Point out each malaria parasite.
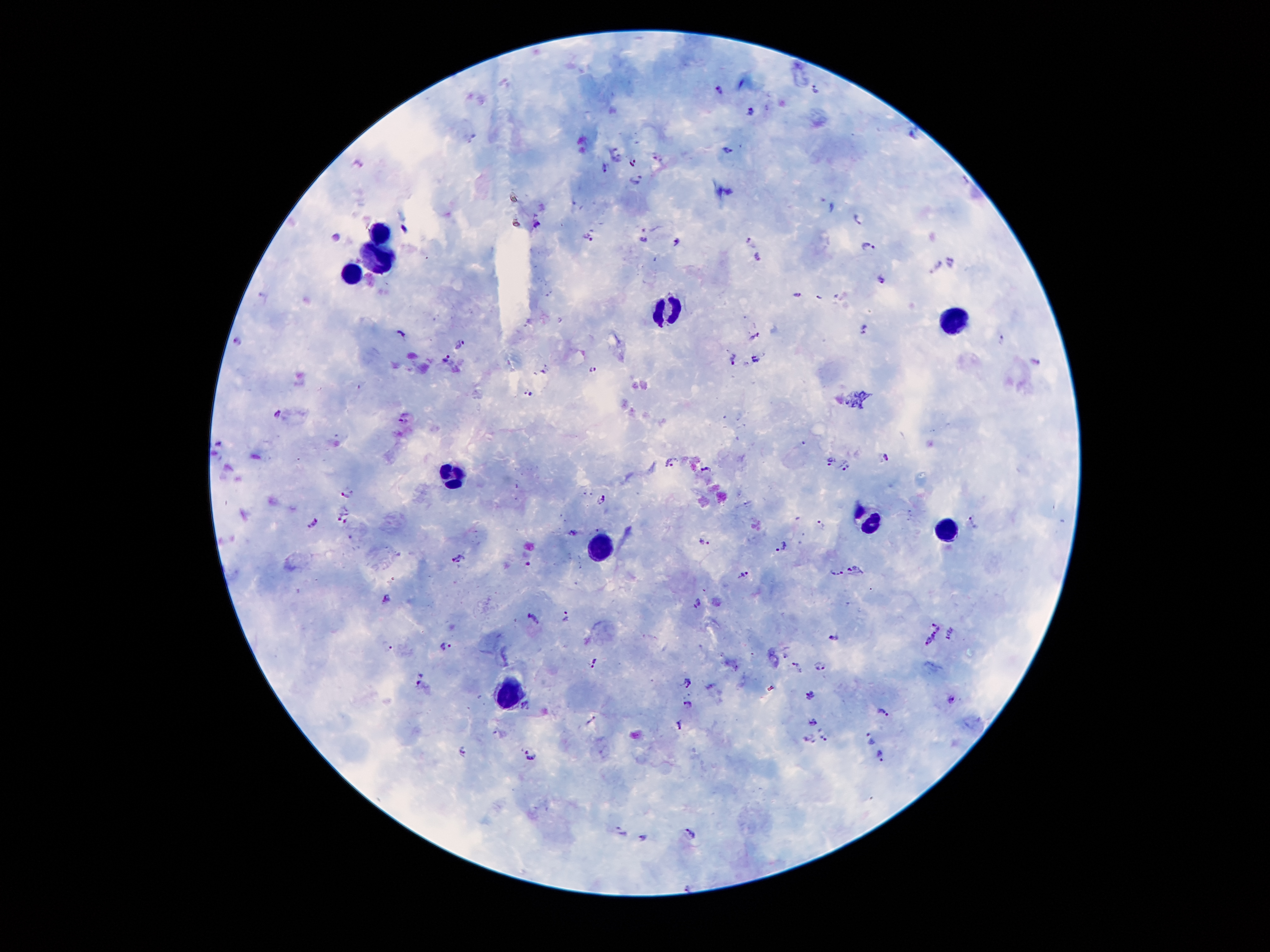
Approximate centers as (x, y) in pixels.
Malaria parasites: (814, 88), (718, 89), (751, 111), (910, 136), (727, 150), (617, 158), (633, 162), (605, 168), (637, 179), (831, 206), (857, 217), (537, 224), (404, 230), (588, 235), (336, 236), (643, 238), (750, 239), (677, 242), (867, 246), (756, 255), (951, 262), (937, 267), (884, 279), (799, 295), (819, 296), (865, 329), (402, 334), (754, 336), (1001, 338), (236, 343), (461, 346), (446, 358), (733, 359), (755, 359), (1036, 361), (593, 369), (546, 371), (530, 392), (277, 413), (405, 418), (221, 445), (885, 456), (830, 461), (848, 461), (671, 462), (842, 469), (706, 470), (345, 496), (601, 498), (339, 513), (346, 521), (974, 522), (314, 523), (820, 524), (574, 533), (705, 542), (782, 546), (459, 559), (528, 564), (855, 569), (837, 572), (743, 574), (387, 597), (698, 602), (566, 616), (532, 617), (936, 624), (951, 634), (834, 635), (934, 636), (926, 644), (387, 645), (446, 647), (785, 656), (594, 663), (815, 665), (797, 666), (824, 667), (687, 680), (422, 685), (711, 685), (810, 695), (953, 698), (688, 702), (524, 704), (882, 713), (591, 720), (813, 723), (679, 725), (870, 736), (823, 737), (810, 738), (461, 750), (531, 756), (880, 757), (622, 833), (691, 834), (643, 837), (689, 887).

leukocyte locations = (381, 228), (378, 265), (346, 271), (665, 312), (950, 320), (451, 471), (864, 525), (943, 525), (599, 549), (507, 693)
field of view = one from this slide
capture = smartphone through the microscope eyepiece
image size = 1270×952 pixels
stain = Giemsa
patient malaria status = infected with Plasmodium falciparum
preparation = thick blood smear
magnification = 100x